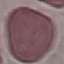
Summary:
  - Malaria status: uninfected
  - Image type: cell patch, automatically extracted from a larger field of view and resized to 64 × 64 pixels
  - Preparation: thin blood film
  - Stain: Giemsa
  - Capture: smartphone camera at the microscope eyepiece